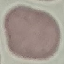

Result: no malaria parasites seen. Acquired by smartphone through the microscope eyepiece. Giemsa stain. Cell patch, automatically extracted from a larger field of view and resized to 64 × 64 pixels. Thin blood film.